Assess the morphology of the red blood cells.
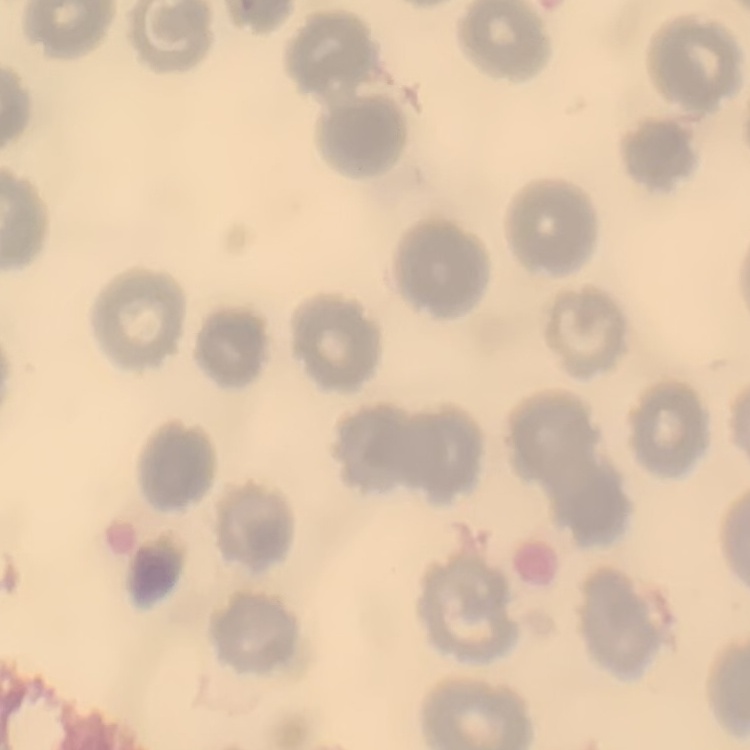

No rouleaux formation.

stain = Field's or Giemsa
image type = square crop of a larger photomicrograph
preparation = thin blood smear